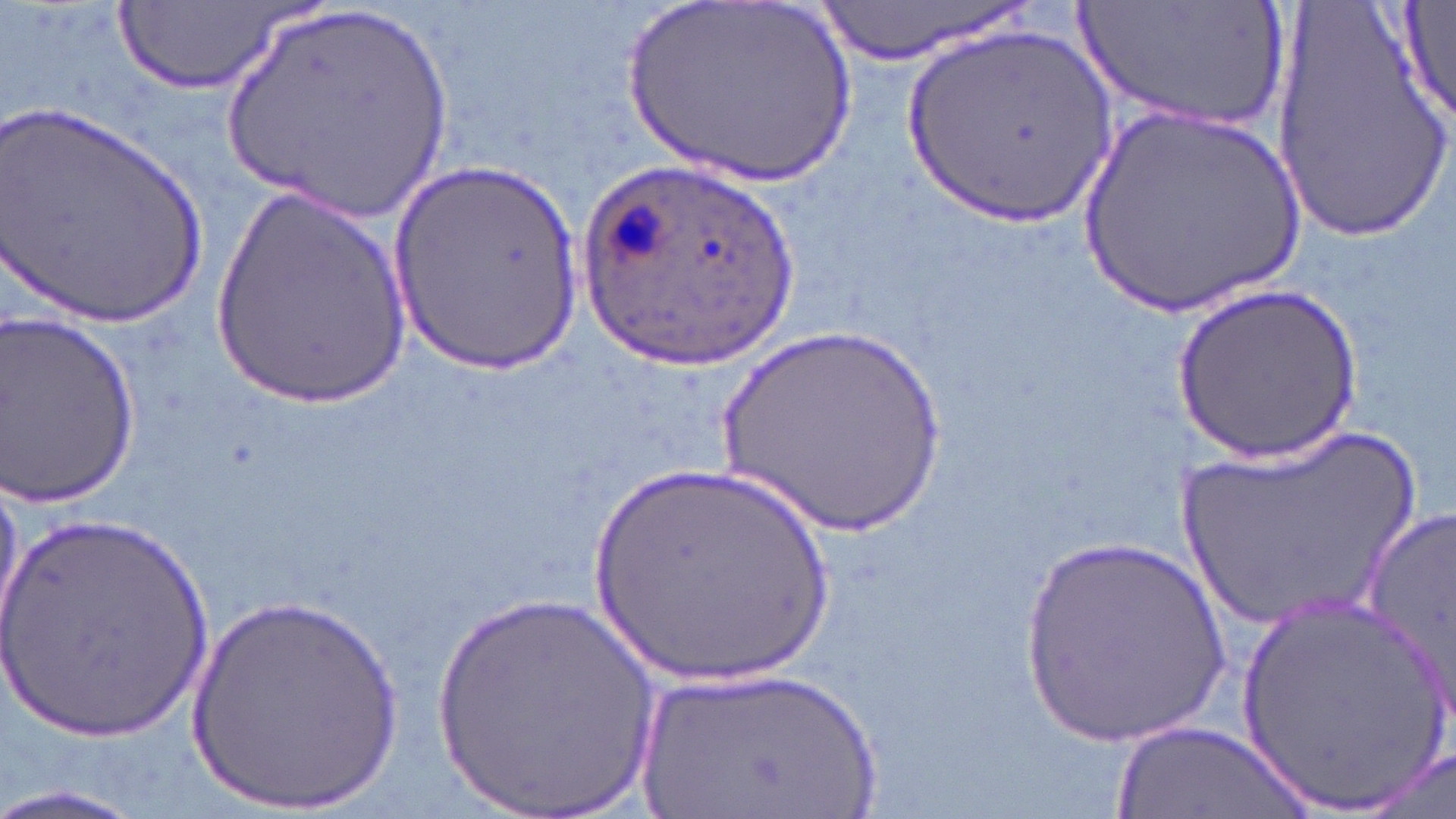
Summary:
  - Coordinate format: approximate bounding boxes as (x1,y1)-(x2,y2) corner pairs in pixels
  - Uninfected red blood cell locations: (1074,0)-(1290,132), (1395,0)-(1455,127), (809,1)-(1035,65), (617,2)-(865,199), (218,3)-(458,228), (113,4)-(310,95), (1267,7)-(1455,243), (897,20)-(1116,229), (0,99)-(214,333), (1072,100)-(1318,323), (390,161)-(587,375), (210,182)-(415,407), (1175,280)-(1362,463), (0,311)-(144,509), (709,317)-(959,546), (1169,421)-(1431,637), (578,455)-(852,698), (1366,498)-(1456,709), (1,508)-(219,740), (1013,527)-(1238,755), (424,591)-(671,819), (181,592)-(410,813), (1229,592)-(1452,815), (625,666)-(889,819), (1109,723)-(1317,817), (1362,744)-(1454,817), (0,782)-(156,819)
  - Plasmodium ovale-infected red blood cell locations: (568,154)-(805,372)
  - Slide-level diagnosis: Plasmodium ovale
  - Preparation: thin blood film
  - Field of view: one of a larger specimen
  - Modality: optical microscopy
  - Magnification: 1000x
  - Stain: May-Grünwald-Giemsa
  - Image size: 1456×819 pixels